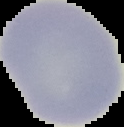

malaria_status: uninfected
image_type: cell region segmented out of the field of view; surrounding area masked to black
preparation: thin blood smear
image_size: 124×127 pixels